Name the parasite shown.
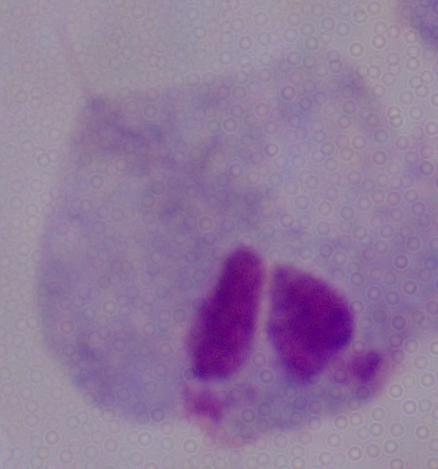
A trichomonad.

Summary:
  - Modality: micrograph
  - Magnification: 1000x